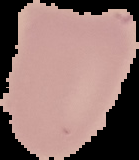

Malaria status: uninfected. From a thin blood film. Cell region segmented out of the field of view; the surrounding area is masked to black. Image is 139×160 pixels.